Assess this cell for malaria.
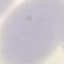
It is uninfected.

Photographed with a smartphone camera at the microscope eyepiece. Automatically extracted cell patch, resized to 64 × 64 pixels. Thin blood smear. Giemsa stain.